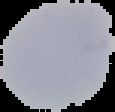
Summary:
  - Preparation: thin blood smear
  - Image size: 115×112 pixels
  - Malaria status: uninfected
  - Image type: segmented cell region on a black background